Locate every Plasmodium falciparum-infected red blood cell.
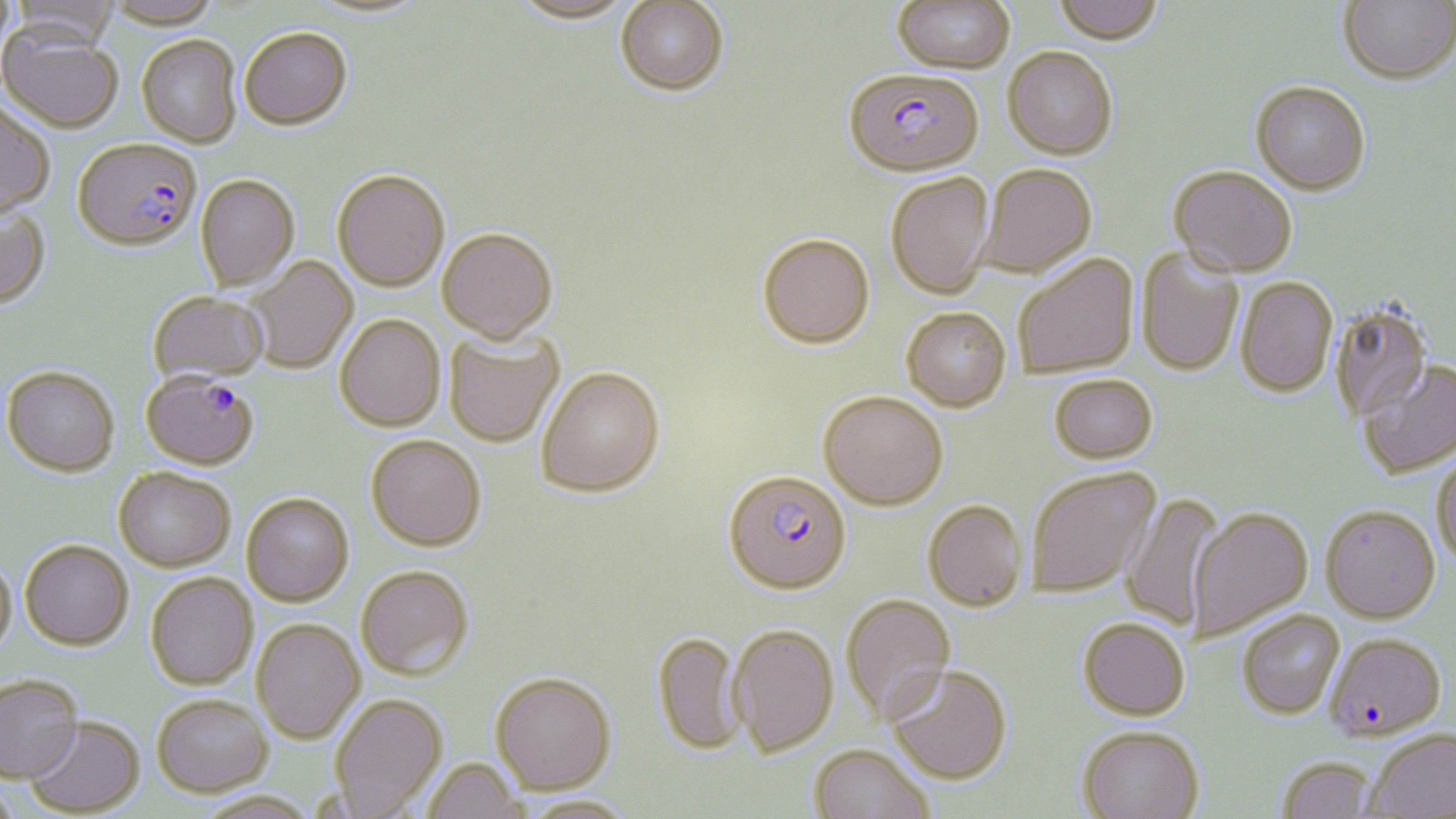

Approximate bounding boxes as named x1/y1/x2/y2 corners in pixels.
Plasmodium falciparum-infected red blood cells: (x1=843, y1=67, x2=985, y2=175), (x1=73, y1=137, x2=201, y2=251), (x1=141, y1=370, x2=261, y2=470), (x1=723, y1=468, x2=852, y2=594), (x1=1326, y1=632, x2=1446, y2=741).

Uninfected red blood cell locations: (x1=102, y1=0, x2=222, y2=28), (x1=508, y1=0, x2=638, y2=25), (x1=1051, y1=0, x2=1165, y2=43), (x1=1339, y1=0, x2=1455, y2=83), (x1=7, y1=1, x2=121, y2=49), (x1=615, y1=1, x2=729, y2=96), (x1=892, y1=1, x2=1015, y2=73), (x1=0, y1=25, x2=124, y2=133), (x1=239, y1=26, x2=353, y2=129), (x1=136, y1=33, x2=242, y2=147), (x1=1002, y1=46, x2=1119, y2=159), (x1=1251, y1=80, x2=1371, y2=194), (x1=0, y1=101, x2=56, y2=217), (x1=977, y1=163, x2=1097, y2=278), (x1=1169, y1=164, x2=1297, y2=276), (x1=332, y1=168, x2=450, y2=290), (x1=884, y1=172, x2=995, y2=299), (x1=196, y1=174, x2=299, y2=290), (x1=0, y1=203, x2=51, y2=308), (x1=437, y1=226, x2=558, y2=341), (x1=757, y1=233, x2=875, y2=347), (x1=1136, y1=246, x2=1244, y2=377), (x1=1012, y1=253, x2=1138, y2=379), (x1=244, y1=256, x2=358, y2=373), (x1=1236, y1=276, x2=1338, y2=397), (x1=147, y1=290, x2=269, y2=383), (x1=1329, y1=301, x2=1433, y2=424), (x1=901, y1=306, x2=1011, y2=411), (x1=335, y1=314, x2=445, y2=431), (x1=444, y1=327, x2=564, y2=447), (x1=1357, y1=360, x2=1456, y2=479), (x1=535, y1=364, x2=665, y2=497), (x1=3, y1=365, x2=119, y2=475), (x1=1049, y1=374, x2=1158, y2=463), (x1=818, y1=390, x2=949, y2=509), (x1=366, y1=434, x2=486, y2=550), (x1=1431, y1=450, x2=1456, y2=571), (x1=1025, y1=465, x2=1162, y2=599), (x1=114, y1=466, x2=236, y2=570), (x1=241, y1=492, x2=354, y2=605), (x1=1120, y1=493, x2=1227, y2=630), (x1=922, y1=499, x2=1028, y2=611), (x1=1320, y1=504, x2=1441, y2=622), (x1=1186, y1=506, x2=1313, y2=640), (x1=20, y1=539, x2=134, y2=649), (x1=0, y1=556, x2=17, y2=659), (x1=355, y1=564, x2=474, y2=679), (x1=146, y1=572, x2=258, y2=689), (x1=840, y1=593, x2=956, y2=724), (x1=1237, y1=609, x2=1345, y2=718), (x1=1078, y1=617, x2=1190, y2=720), (x1=252, y1=618, x2=365, y2=743), (x1=727, y1=623, x2=839, y2=757), (x1=652, y1=631, x2=747, y2=755), (x1=885, y1=663, x2=1013, y2=784), (x1=490, y1=670, x2=616, y2=794), (x1=0, y1=673, x2=82, y2=781), (x1=329, y1=692, x2=447, y2=818), (x1=152, y1=693, x2=272, y2=795), (x1=24, y1=716, x2=145, y2=817), (x1=1076, y1=725, x2=1205, y2=819), (x1=1365, y1=727, x2=1456, y2=818), (x1=809, y1=743, x2=936, y2=819), (x1=1275, y1=754, x2=1379, y2=818), (x1=421, y1=757, x2=527, y2=819), (x1=1, y1=783, x2=24, y2=819), (x1=518, y1=794, x2=637, y2=819). Slide-level diagnosis: Plasmodium falciparum. Image is 1456×819 pixels. Thin blood film. Single field of view. Optical microscopy. Captured at 1000x magnification. May-Grünwald-Giemsa stain.